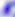
Summary:
  - Identification: Toxoplasma gondii
  - Modality: micrograph
  - Magnification: 400x